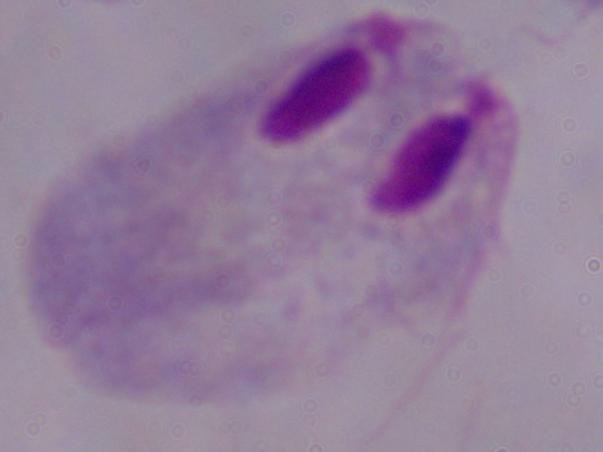

Summary:
  - Modality: photomicrograph
  - Magnification: 1000x
  - Identification: trichomonad